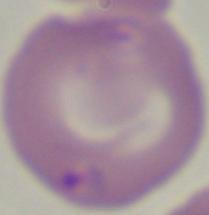
identification = Babesia
modality = micrograph
magnification = 1000x